Assess this cell for malaria.
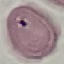
Uninfected.

Summary:
  - Preparation: thin smear
  - Image type: automatically extracted cell patch, resized to 64 × 64 pixels
  - Capture: smartphone through the microscope eyepiece
  - Stain: Giemsa